Report the malaria status of this cell.
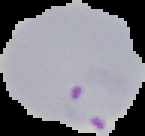

Parasitized.

Summary:
  - Image type: segmented cell region on a black background
  - Image size: 145×136 pixels
  - Preparation: thin blood film